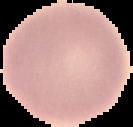

Summary:
  - Image type: segmented cell region with the area outside set to black
  - Image size: 133×127 pixels
  - Result: negative for Plasmodium parasites
  - Preparation: thin blood film